Identify the parasite.
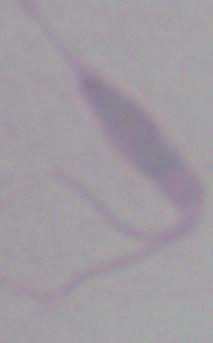

This is Leishmania.

modality = photomicrograph
magnification = 1000x